Classify this cell by malaria status.
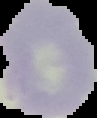

Uninfected.

Summary:
  - Image size: 97×118 pixels
  - Image type: segmented cell region on a black background
  - Preparation: thin blood smear